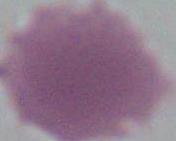
Summary:
  - Identification: erythrocyte
  - Magnification: 1000x
  - Modality: photomicrograph